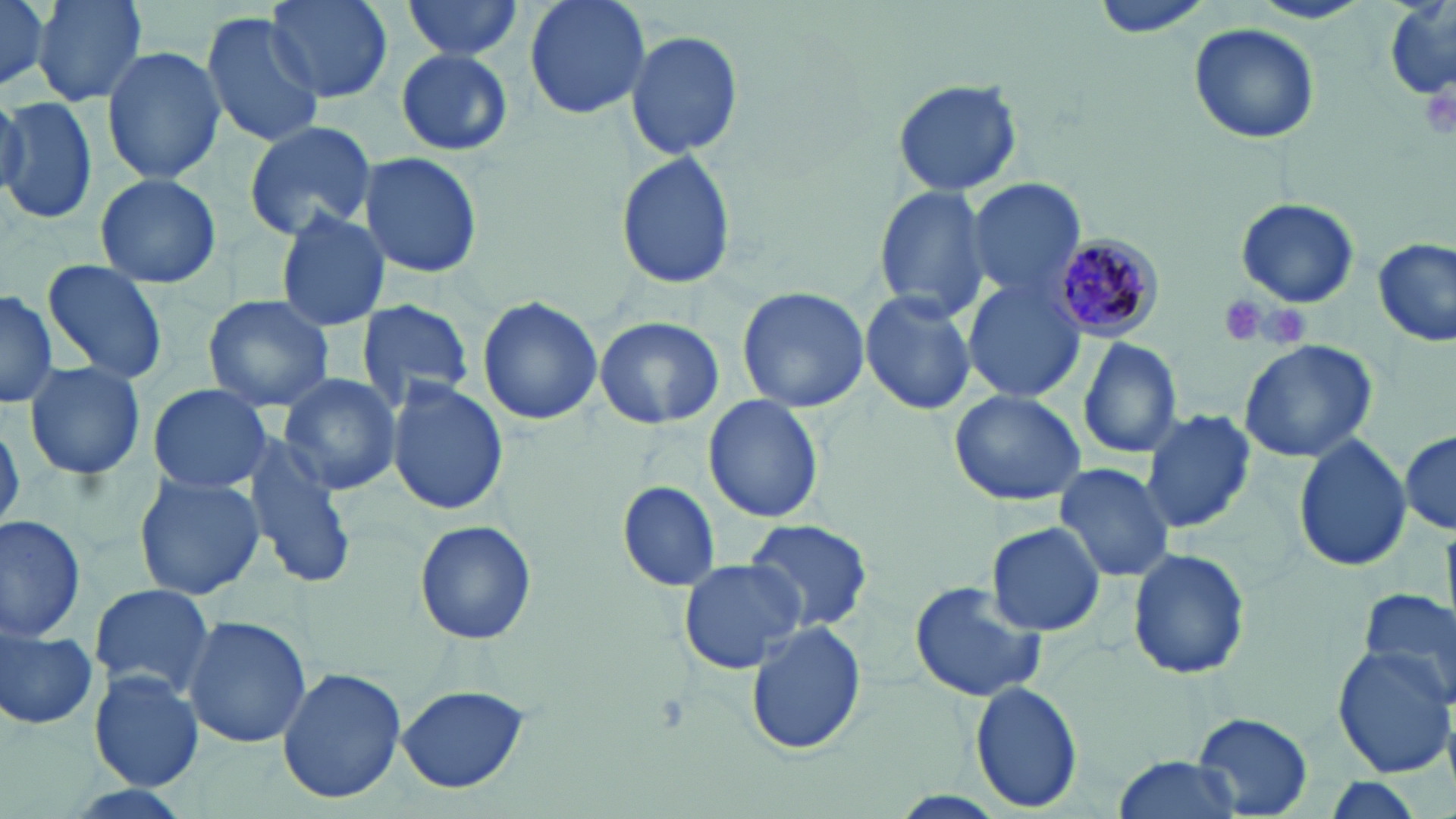
slide-level diagnosis = Plasmodium malariae
magnification = 1000x
preparation = thin blood smear
image size = 1456×819 pixels
Plasmodium malariae-infected red blood cell locations = approximate bounding boxes as [x1, y1, x2, y2] in pixels: [1055, 231, 1170, 344]
stain = May-Grünwald-Giemsa
modality = light microscopy
field of view = one of a larger specimen
uninfected red blood cell locations = approximate bounding boxes as [x1, y1, x2, y2] in pixels: [0, 0, 53, 92], [33, 0, 148, 106], [264, 0, 394, 104], [401, 0, 525, 60], [522, 0, 653, 123], [1250, 0, 1374, 25], [1091, 2, 1213, 38], [1383, 5, 1453, 103], [200, 10, 326, 147], [1190, 24, 1320, 143], [624, 26, 743, 163], [101, 45, 226, 183], [395, 48, 513, 157], [892, 77, 1022, 198], [0, 95, 98, 226], [243, 120, 377, 240], [359, 151, 484, 281], [615, 151, 738, 290], [93, 172, 222, 288], [966, 176, 1088, 302], [872, 184, 993, 323], [1236, 198, 1360, 308], [275, 207, 392, 331], [1373, 238, 1454, 346], [42, 259, 169, 387], [965, 280, 1089, 402], [736, 286, 870, 414], [0, 287, 58, 408], [858, 289, 979, 416], [202, 295, 334, 412], [477, 295, 604, 428], [353, 299, 475, 413], [594, 317, 724, 430], [1078, 337, 1182, 459], [1238, 338, 1379, 463], [21, 360, 147, 483], [278, 373, 402, 497], [386, 379, 509, 517], [147, 382, 272, 494], [947, 391, 1089, 506], [703, 393, 824, 524], [1139, 408, 1255, 538], [1, 416, 23, 534], [1401, 430, 1455, 533], [1293, 435, 1414, 574], [241, 438, 357, 587], [1053, 463, 1174, 583], [133, 472, 266, 602], [616, 480, 722, 592], [0, 514, 88, 641], [744, 518, 877, 637], [414, 521, 536, 646], [986, 521, 1106, 637], [1127, 547, 1252, 682], [677, 559, 806, 674], [909, 580, 1048, 703], [86, 583, 216, 700], [1356, 588, 1456, 705], [183, 615, 312, 749], [0, 620, 99, 732], [744, 623, 868, 756], [1331, 645, 1455, 776], [277, 667, 407, 804], [88, 672, 205, 790], [969, 682, 1082, 811], [396, 683, 532, 795], [1193, 713, 1313, 816], [1113, 754, 1241, 819]
platelet locations = approximate bounding boxes as [x1, y1, x2, y2] in pixels: [1420, 81, 1455, 142], [1214, 293, 1269, 346], [1253, 302, 1313, 349]